Outline each blood parasite and name the species.
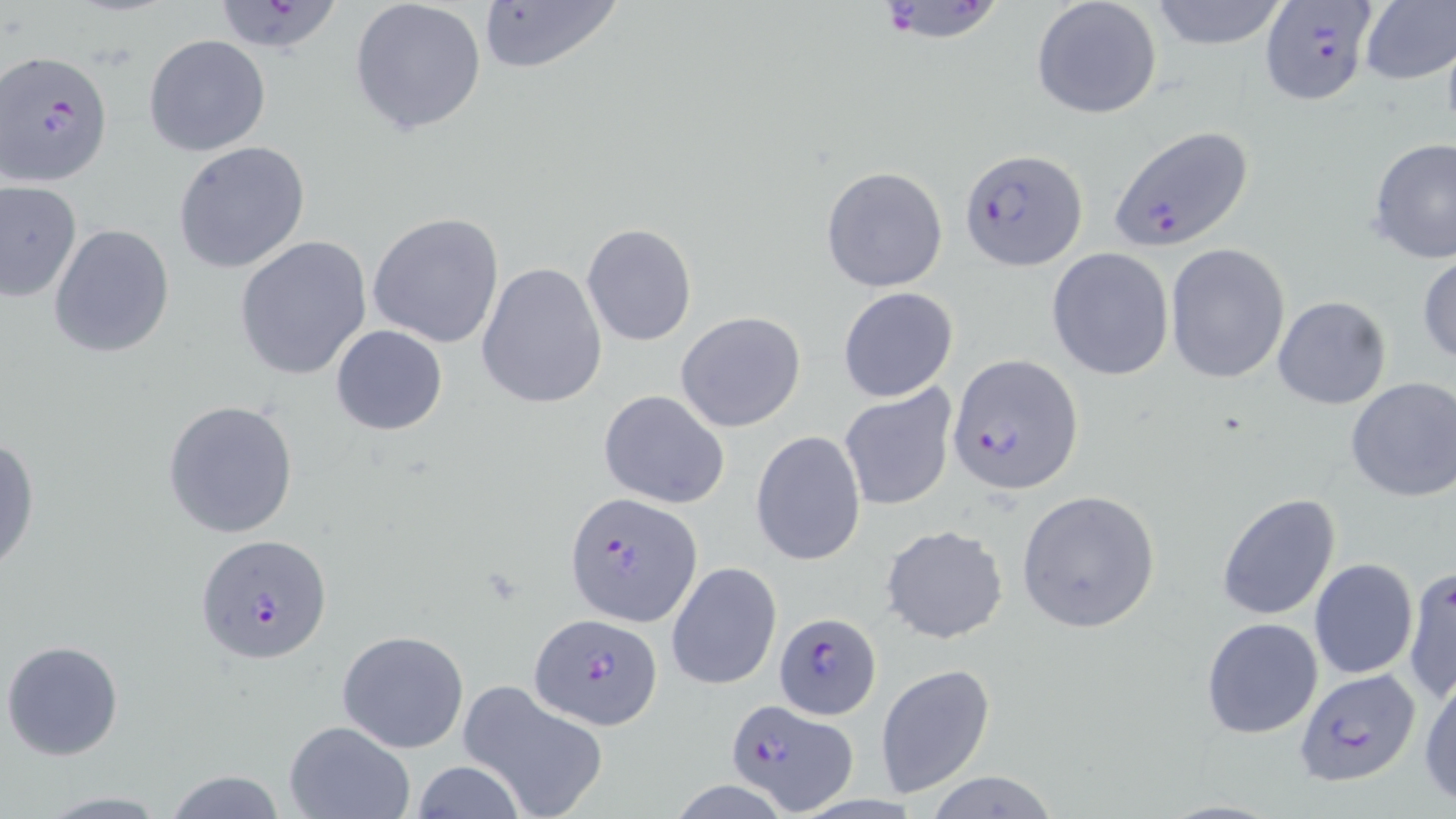
Approximate bounding boxes as (x1,y1)-(x2,y2) corner pairs in pixels.
Plasmodium falciparum-infected red blood cells: (885,1)-(1001,50), (1259,1)-(1377,107), (220,2)-(342,55), (2,49)-(114,186), (1107,124)-(1255,253), (958,148)-(1087,271), (948,355)-(1084,496), (566,492)-(703,626), (196,533)-(333,664), (773,612)-(882,720), (529,613)-(663,731), (1295,669)-(1422,786), (725,699)-(857,813).
No Plasmodium ovale, Plasmodium malariae, Plasmodium vivax, Babesia divergens, or Trypanosoma brucei observed.

Uninfected red blood cell locations: (349,0)-(489,138), (475,0)-(626,77), (1031,0)-(1163,121), (1147,0)-(1291,51), (1357,2)-(1456,85), (143,35)-(271,157), (1367,138)-(1456,264), (172,141)-(311,274), (820,165)-(948,292), (2,181)-(81,301), (367,211)-(506,349), (581,223)-(697,347), (49,224)-(175,360), (233,235)-(372,381), (1164,244)-(1290,382), (1047,248)-(1174,381), (1417,249)-(1456,367), (475,261)-(609,411), (838,286)-(959,403), (1272,295)-(1392,410), (675,311)-(806,432), (329,324)-(448,436), (1344,378)-(1456,502), (839,385)-(957,511), (597,389)-(730,509), (162,399)-(300,539), (853,401)-(977,589), (751,432)-(866,566), (0,437)-(39,576), (1015,490)-(1161,634), (1216,492)-(1342,621), (882,525)-(1007,645), (1308,559)-(1419,679), (666,561)-(782,691), (1403,564)-(1456,705), (1201,617)-(1323,739), (336,629)-(471,753), (2,639)-(125,760), (877,663)-(994,799), (1417,670)-(1456,806), (457,680)-(609,819), (284,720)-(416,819), (410,761)-(528,819), (159,770)-(294,818), (925,771)-(1059,818), (29,792)-(180,817). Slide-level diagnosis: Plasmodium falciparum. Single field of view. Image is 1456×819 pixels. Thin blood smear. Optical microscopy. 1000x magnification. May-Grünwald-Giemsa-stained preparation.